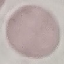 Malaria status: uninfected. Thin blood film. Photographed with a smartphone camera at the microscope eyepiece. Cell patch, automatically extracted from a larger field of view and resized to 64 × 64 pixels. Giemsa-stained preparation.